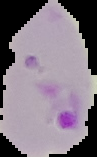
Summary:
  - Malaria status: parasitized
  - Preparation: thin blood film
  - Image size: 97×157 pixels
  - Image type: cell region segmented out of the field of view; surrounding area masked to black